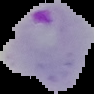
{
  "malaria_status": "parasitized",
  "preparation": "thin blood smear",
  "image_size": "94×94 pixels",
  "image_type": "segmented cell region with the area outside set to black"
}